Locate every blood parasite and identify its species.
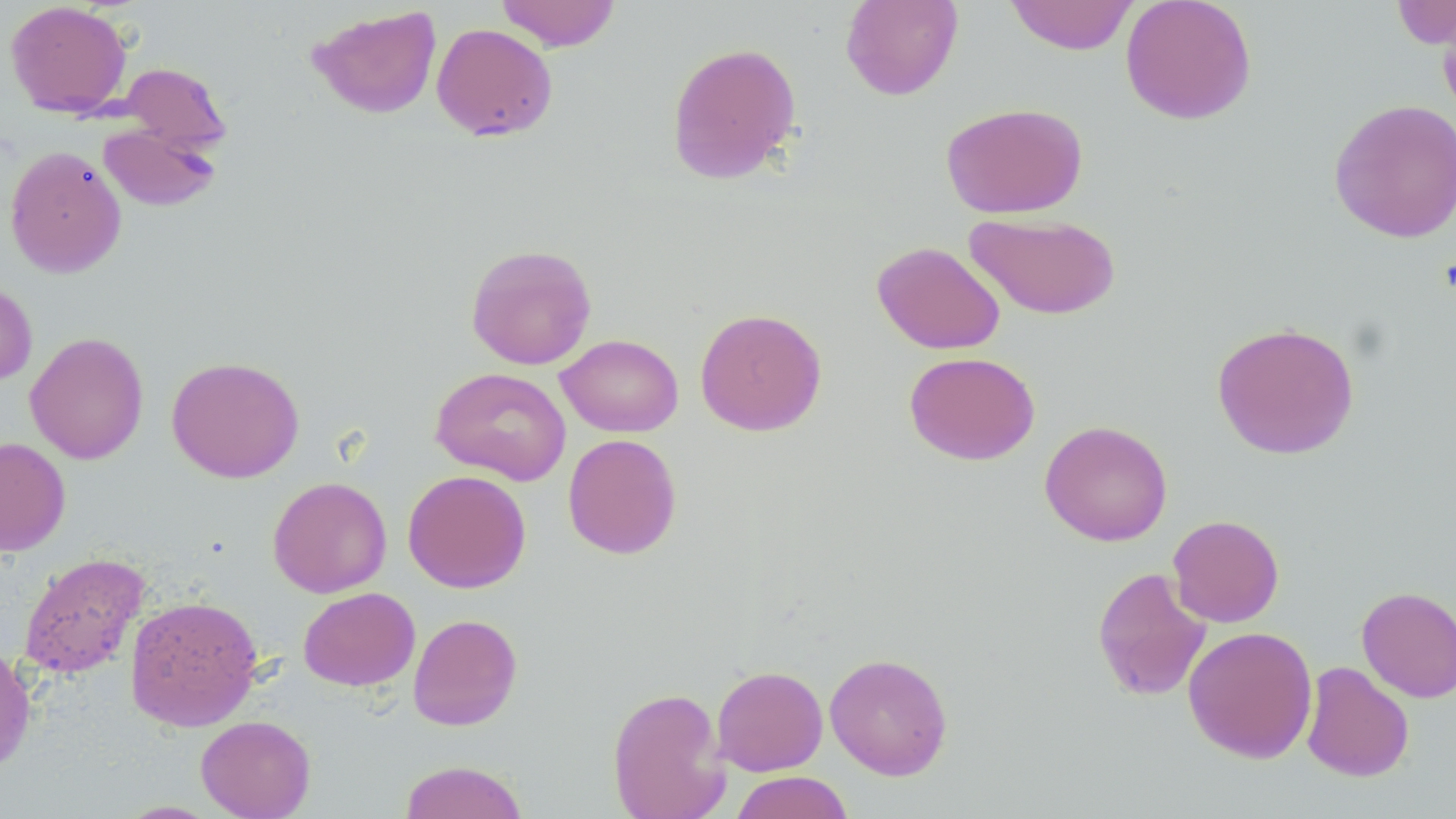
No blood parasites seen.

Approximate bounding boxes as named x1/y1/x2/y2 corners in pixels. Uninfected red blood cell locations: (x1=494, y1=0, x2=621, y2=51), (x1=840, y1=0, x2=963, y2=101), (x1=1005, y1=0, x2=1138, y2=55), (x1=1120, y1=0, x2=1257, y2=125), (x1=5, y1=1, x2=132, y2=118), (x1=1391, y1=1, x2=1456, y2=49), (x1=307, y1=4, x2=442, y2=120), (x1=1437, y1=8, x2=1456, y2=122), (x1=431, y1=22, x2=558, y2=141), (x1=666, y1=41, x2=802, y2=185), (x1=118, y1=63, x2=231, y2=154), (x1=1328, y1=98, x2=1456, y2=243), (x1=941, y1=101, x2=1088, y2=218), (x1=98, y1=123, x2=222, y2=212), (x1=5, y1=145, x2=127, y2=278), (x1=964, y1=212, x2=1121, y2=320), (x1=872, y1=241, x2=1005, y2=354), (x1=465, y1=243, x2=597, y2=370), (x1=0, y1=279, x2=37, y2=387), (x1=695, y1=307, x2=827, y2=436), (x1=1211, y1=321, x2=1360, y2=460), (x1=25, y1=331, x2=149, y2=464), (x1=556, y1=334, x2=683, y2=437), (x1=904, y1=351, x2=1040, y2=465), (x1=166, y1=355, x2=305, y2=483), (x1=430, y1=367, x2=571, y2=485), (x1=1040, y1=419, x2=1173, y2=546), (x1=562, y1=433, x2=683, y2=559), (x1=0, y1=437, x2=71, y2=556), (x1=402, y1=469, x2=531, y2=593), (x1=267, y1=476, x2=392, y2=598), (x1=1168, y1=515, x2=1284, y2=627), (x1=19, y1=552, x2=149, y2=678), (x1=1091, y1=566, x2=1213, y2=702), (x1=298, y1=587, x2=420, y2=691), (x1=1356, y1=587, x2=1456, y2=702), (x1=125, y1=594, x2=263, y2=731), (x1=407, y1=613, x2=523, y2=732), (x1=1183, y1=625, x2=1318, y2=763), (x1=0, y1=643, x2=37, y2=776), (x1=824, y1=652, x2=953, y2=780), (x1=1300, y1=661, x2=1415, y2=782), (x1=711, y1=665, x2=828, y2=776), (x1=606, y1=687, x2=730, y2=819), (x1=196, y1=715, x2=316, y2=819), (x1=398, y1=759, x2=529, y2=819), (x1=729, y1=771, x2=855, y2=819). Slide-level diagnosis: negative for blood parasites. Optical microscopy. Image is 1456×819 pixels. 1000x magnification. Single field of view. Thin blood smear. May-Grünwald-Giemsa stain.